Report the malaria status of this cell.
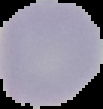

It is uninfected.

Summary:
  - Preparation: thin blood smear
  - Image size: 103×109 pixels
  - Image type: segmented cell region on a black background